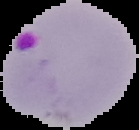
Summary:
  - Image type: segmented cell region on a black background
  - Result: malaria parasites identified
  - Preparation: thin blood smear
  - Image size: 139×130 pixels